Give the position of every malaria parasite.
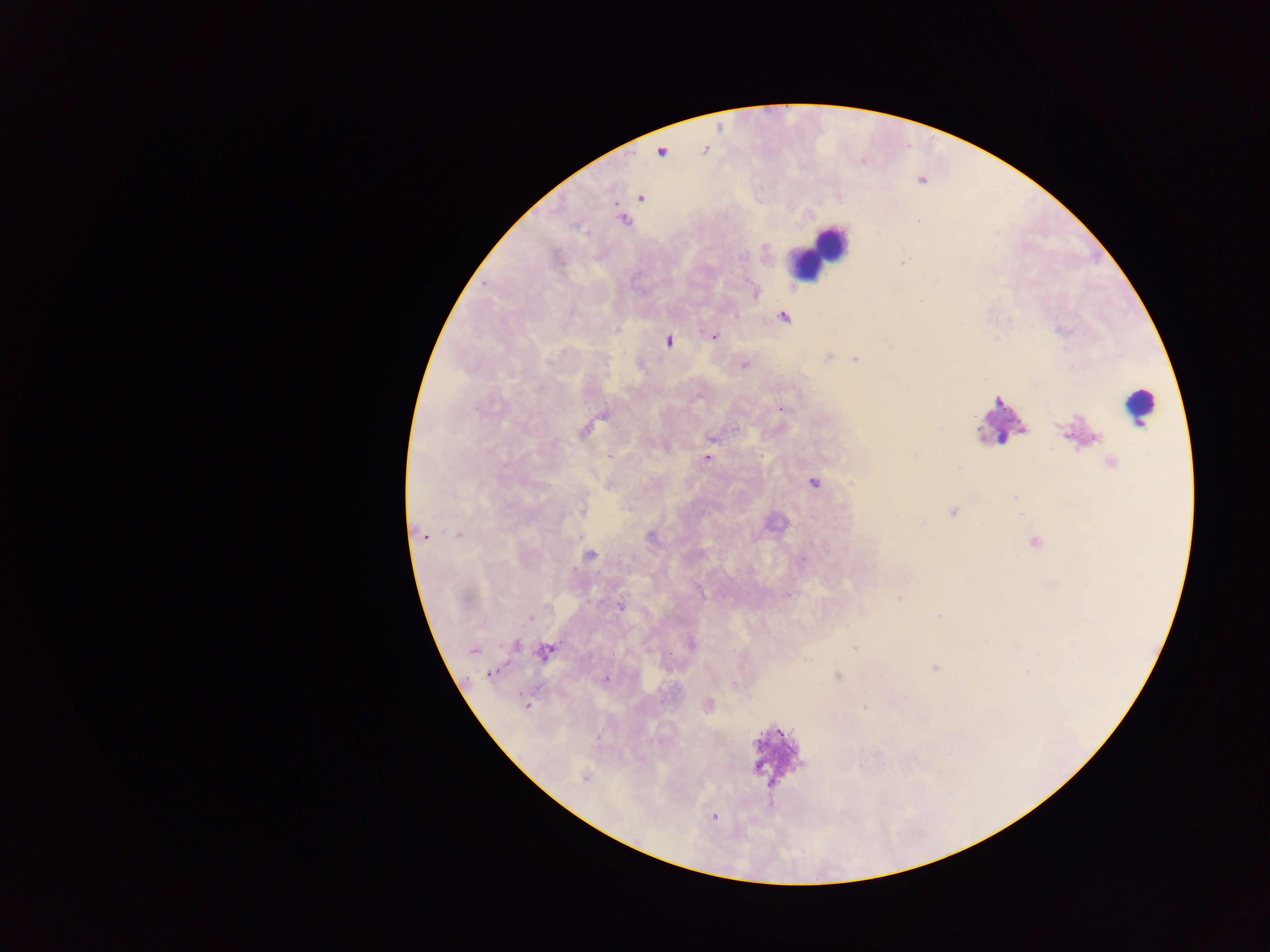
Approximate centers as [x, y] in pixels.
Malaria parasites: [640, 197], [623, 220], [919, 221], [783, 317], [714, 335], [669, 341], [827, 357], [855, 358], [744, 365], [779, 409], [603, 415], [711, 439], [707, 458], [813, 483], [584, 509], [953, 511], [921, 525], [458, 533], [424, 536], [1035, 543], [590, 555], [804, 560], [788, 595], [899, 597], [621, 606], [939, 616], [531, 617], [691, 644], [516, 645], [854, 648], [473, 651], [544, 652], [936, 668], [491, 674], [838, 676], [605, 680], [734, 684], [526, 705], [708, 705], [864, 706], [584, 778], [714, 817].

Leukocyte locations: [661, 151], [827, 244], [810, 259], [1137, 406], [998, 418], [774, 751]. Thick blood film. Sample from Ghana. Image is 1270×952 pixels. Photographed through a microscope with a mobile-phone camera. Single field of view.